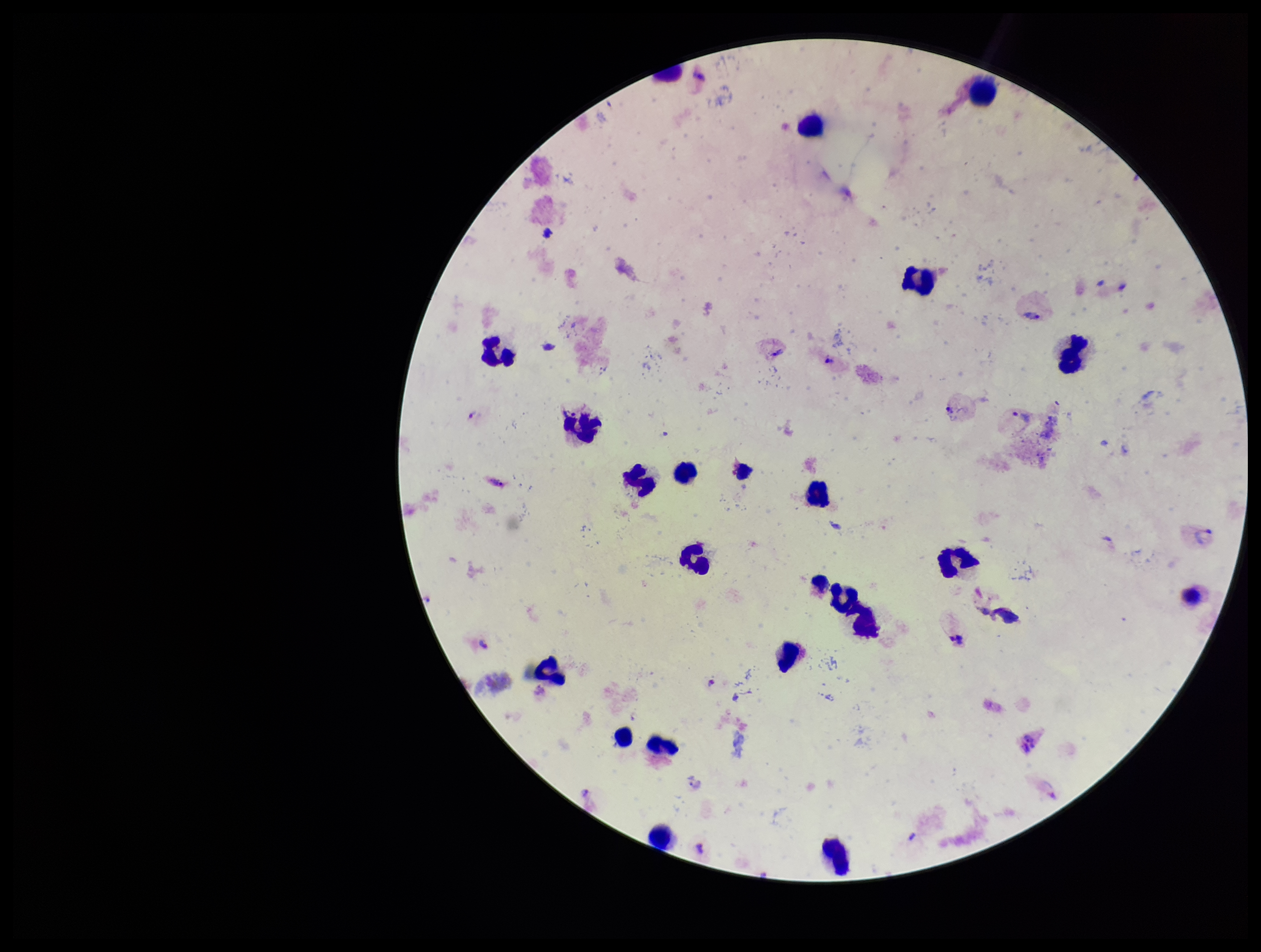

Summary:
  - Stain: Giemsa
  - Leukocyte count: 21
  - Preparation: thick
  - Image size: 1261×952 pixels
  - Capture: smartphone photograph through the microscope eyepiece
  - Plasmodium parasites: seen
  - Field of view: one from this slide
  - Species reported for this patient: Plasmodium vivax
  - Parasite count: 4
  - Patient malaria status: positive